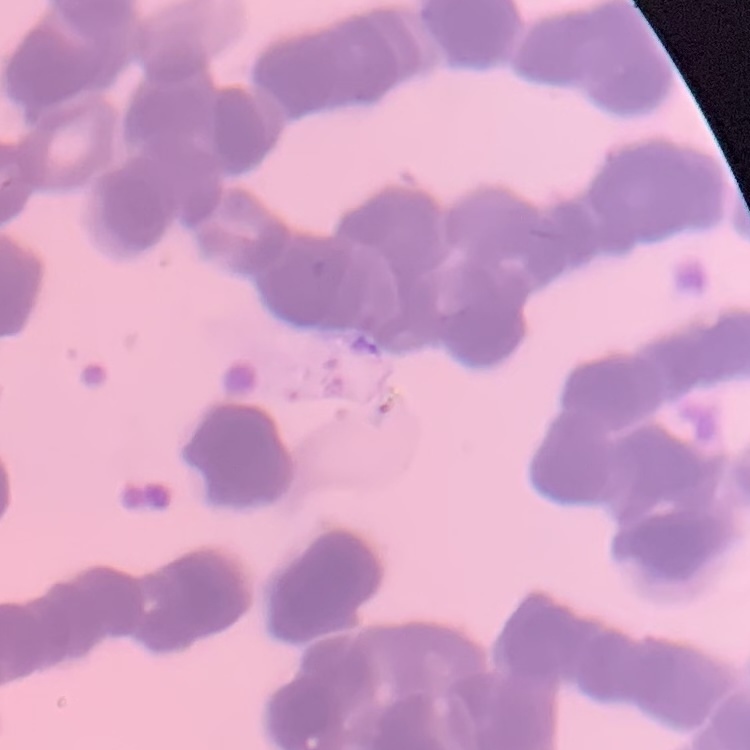 The erythrocytes show rouleaux formation. Square crop of a larger photomicrograph. Stained with either Field's or Giemsa. Thin blood smear.